Name the cell type shown.
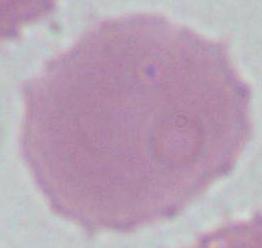
An erythrocyte.

{
  "modality": "micrograph",
  "magnification": "1000x"
}